State which parasite is depicted.
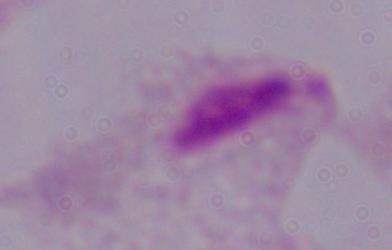
This is a trichomonad.

Summary:
  - Magnification: 1000x
  - Modality: photomicrograph